Give the position of every Plasmodium parasite.
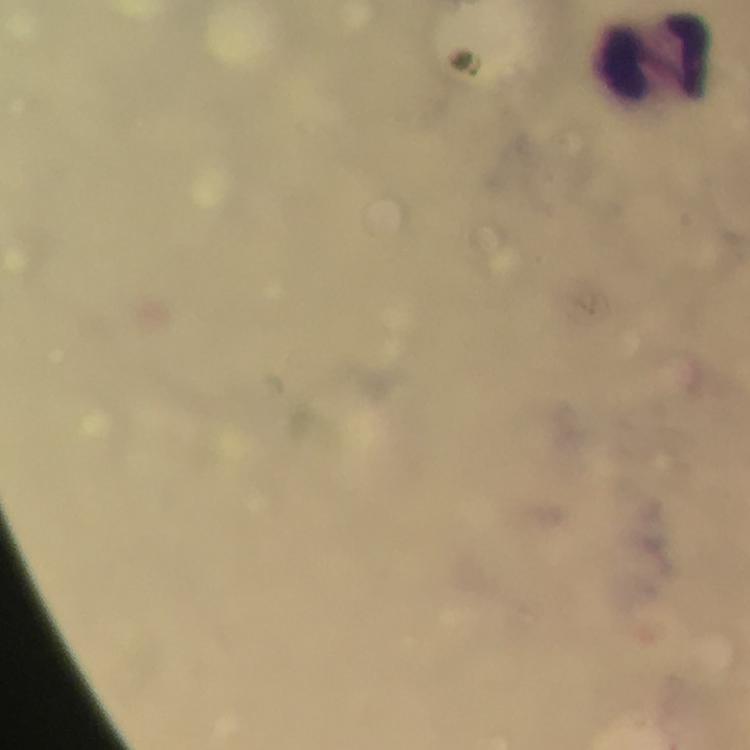
No Plasmodium parasites seen.

Approximate centers as [x, y] in pixels. Leukocyte locations: [656, 56]. Thick blood smear. Photographed with a smartphone mounted on the microscope. Cropped region of a single field of view. From a malaria diagnostic workup. 100x magnification. Immersion oil was used. Giemsa-stained preparation. Image is 750×750 pixels.